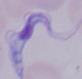

magnification: 1000x
modality: micrograph
identification: trypanosome